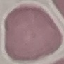 Result: no malaria parasites seen. Giemsa stain. Thin blood film. Cell patch, automatically extracted from a larger field of view and resized to 64 × 64 pixels. Acquired by smartphone through the microscope eyepiece.